Point out each malaria parasite.
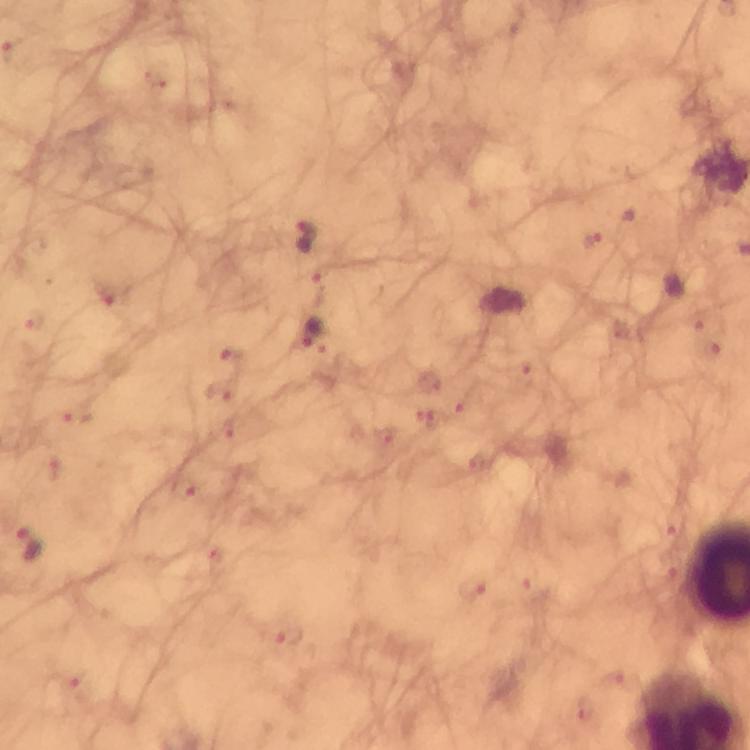

Approximate centers as (x, y) in pixels.
Malaria parasites: (303, 234), (309, 333), (28, 543).

Photographed through the microscope with a smartphone camera. Image is 750×750 pixels. Immersion oil was used. Thick blood film. At 100x magnification. Giemsa-stained preparation. A crop from one field of view. From a malaria diagnostic workup.